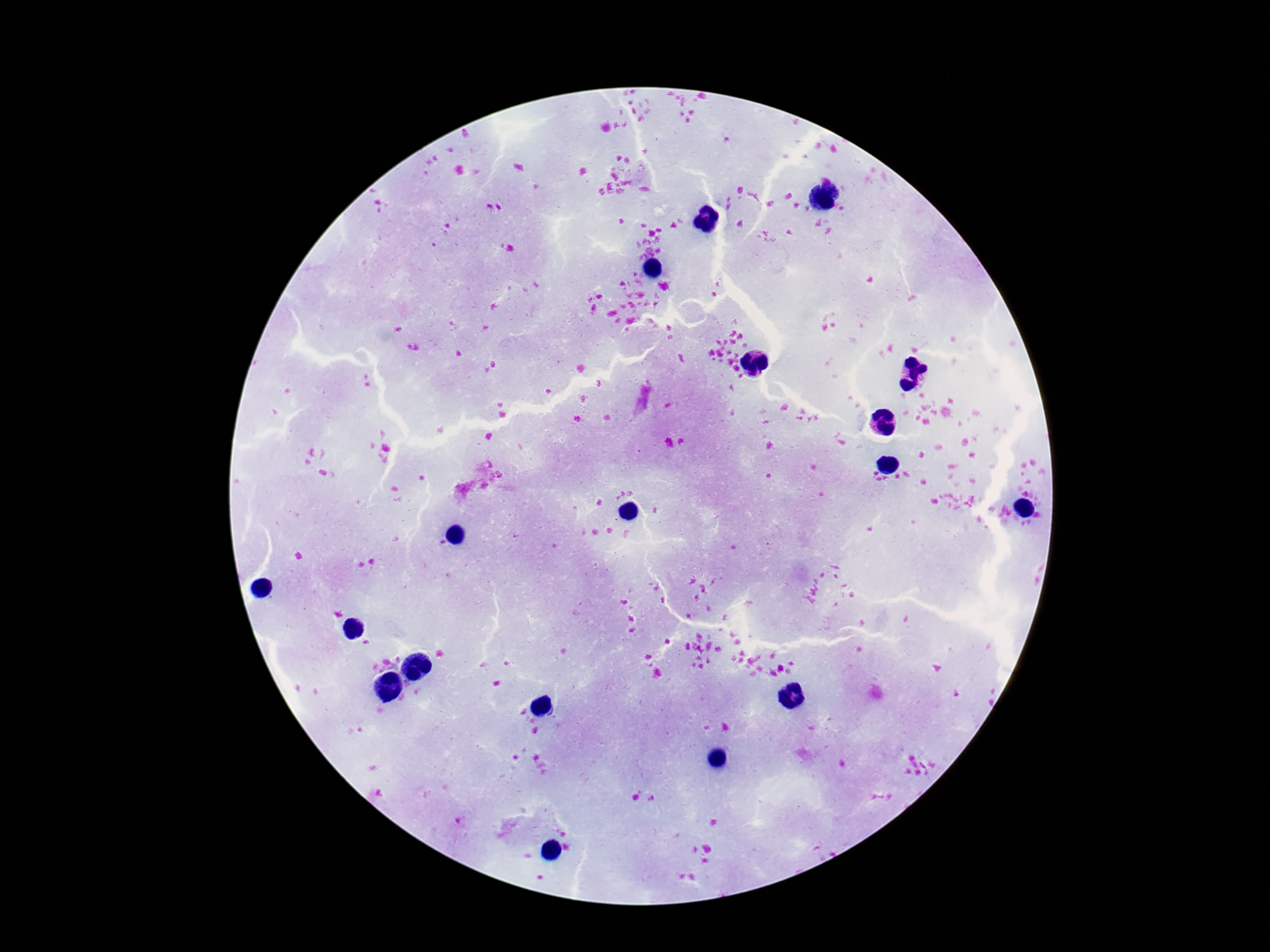
{
  "image_size": "1270×952 pixels",
  "patient_malaria_status": "negative",
  "capture": "smartphone camera through the microscope eyepiece",
  "field_of_view": "one from this slide",
  "leukocyte_locations": "approximate object centers, in pixels from the top-left corner: (x=719, y=99), (x=553, y=190), (x=729, y=243), (x=481, y=255), (x=882, y=267), (x=853, y=288), (x=914, y=327), (x=1007, y=362), (x=813, y=414), (x=642, y=440), (x=247, y=444), (x=383, y=486), (x=386, y=531), (x=359, y=577), (x=522, y=594), (x=618, y=683), (x=563, y=731), (x=450, y=756)",
  "preparation": "thick blood smear",
  "magnification": "100x",
  "stain": "Giemsa"
}